Locate every Plasmodium ovale-infected red blood cell.
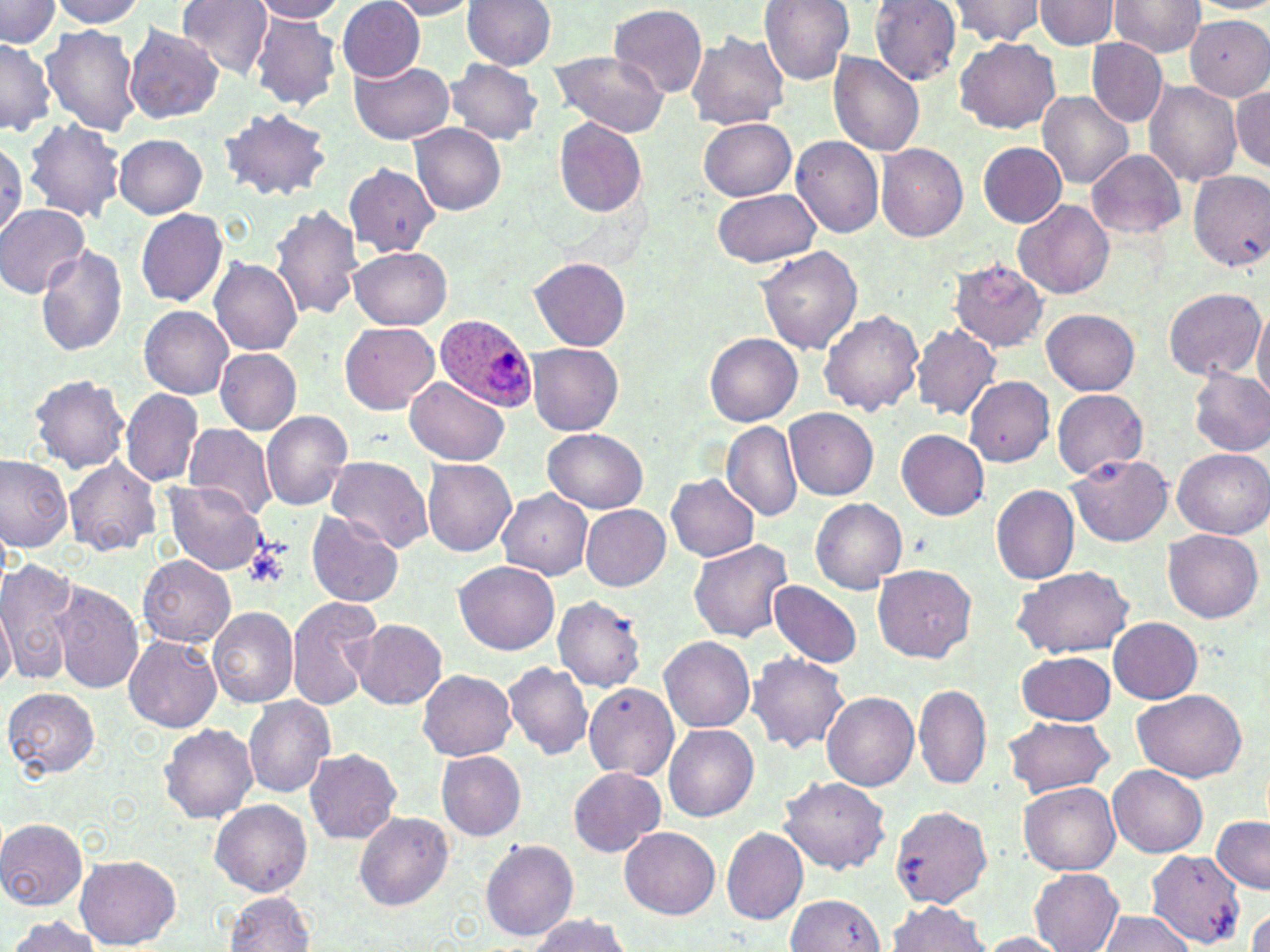

Approximate bounding boxes as named x1/y1/x2/y2 corners in pixels.
Plasmodium ovale-infected red blood cells: (x1=432, y1=313, x2=535, y2=414).

Uninfected red blood cell locations: (x1=176, y1=0, x2=274, y2=78), (x1=250, y1=0, x2=348, y2=23), (x1=383, y1=0, x2=482, y2=20), (x1=461, y1=0, x2=556, y2=70), (x1=759, y1=0, x2=855, y2=84), (x1=942, y1=0, x2=1049, y2=46), (x1=0, y1=1, x2=61, y2=49), (x1=49, y1=1, x2=148, y2=28), (x1=337, y1=1, x2=425, y2=81), (x1=870, y1=1, x2=962, y2=84), (x1=1035, y1=1, x2=1121, y2=49), (x1=1109, y1=1, x2=1205, y2=58), (x1=1187, y1=1, x2=1270, y2=14), (x1=609, y1=4, x2=708, y2=99), (x1=251, y1=6, x2=427, y2=99), (x1=249, y1=12, x2=341, y2=111), (x1=1185, y1=15, x2=1269, y2=99), (x1=41, y1=24, x2=142, y2=136), (x1=123, y1=24, x2=225, y2=124), (x1=686, y1=31, x2=789, y2=132), (x1=0, y1=37, x2=55, y2=136), (x1=954, y1=37, x2=1059, y2=133), (x1=1087, y1=39, x2=1167, y2=127), (x1=547, y1=48, x2=672, y2=137), (x1=828, y1=52, x2=926, y2=155), (x1=446, y1=59, x2=543, y2=145), (x1=352, y1=61, x2=454, y2=143), (x1=1143, y1=81, x2=1243, y2=186), (x1=1231, y1=86, x2=1270, y2=170), (x1=1039, y1=91, x2=1133, y2=190), (x1=217, y1=108, x2=333, y2=202), (x1=23, y1=117, x2=124, y2=220), (x1=699, y1=118, x2=797, y2=201), (x1=554, y1=119, x2=648, y2=216), (x1=410, y1=123, x2=506, y2=215), (x1=113, y1=134, x2=207, y2=218), (x1=789, y1=136, x2=884, y2=239), (x1=0, y1=138, x2=24, y2=236), (x1=978, y1=142, x2=1066, y2=226), (x1=876, y1=143, x2=968, y2=242), (x1=1087, y1=149, x2=1185, y2=240), (x1=343, y1=163, x2=440, y2=258), (x1=1188, y1=171, x2=1270, y2=272), (x1=710, y1=190, x2=821, y2=267), (x1=1013, y1=199, x2=1113, y2=300), (x1=0, y1=202, x2=91, y2=298), (x1=270, y1=204, x2=366, y2=321), (x1=135, y1=208, x2=227, y2=308), (x1=36, y1=245, x2=128, y2=356), (x1=756, y1=246, x2=862, y2=355), (x1=349, y1=247, x2=451, y2=329), (x1=209, y1=258, x2=302, y2=356), (x1=531, y1=258, x2=632, y2=350), (x1=949, y1=259, x2=1049, y2=353), (x1=1162, y1=287, x2=1267, y2=383), (x1=1252, y1=304, x2=1270, y2=407), (x1=139, y1=306, x2=232, y2=400), (x1=818, y1=309, x2=923, y2=415), (x1=1042, y1=309, x2=1139, y2=394), (x1=341, y1=322, x2=439, y2=415), (x1=911, y1=323, x2=1001, y2=421), (x1=704, y1=331, x2=802, y2=426), (x1=526, y1=344, x2=623, y2=436), (x1=215, y1=348, x2=302, y2=434), (x1=1189, y1=368, x2=1270, y2=456), (x1=26, y1=373, x2=131, y2=473), (x1=405, y1=376, x2=508, y2=465), (x1=963, y1=377, x2=1053, y2=466), (x1=121, y1=389, x2=205, y2=486), (x1=1052, y1=389, x2=1149, y2=479), (x1=785, y1=408, x2=878, y2=498), (x1=260, y1=411, x2=354, y2=511), (x1=723, y1=421, x2=800, y2=520), (x1=181, y1=422, x2=277, y2=521), (x1=543, y1=428, x2=648, y2=513), (x1=897, y1=430, x2=989, y2=520), (x1=1173, y1=449, x2=1269, y2=538), (x1=0, y1=453, x2=72, y2=552), (x1=324, y1=455, x2=433, y2=554), (x1=1068, y1=455, x2=1172, y2=545), (x1=64, y1=458, x2=162, y2=556), (x1=423, y1=458, x2=516, y2=557), (x1=666, y1=473, x2=759, y2=562), (x1=166, y1=482, x2=265, y2=574), (x1=992, y1=485, x2=1081, y2=582), (x1=497, y1=489, x2=593, y2=580), (x1=810, y1=498, x2=907, y2=594), (x1=581, y1=505, x2=671, y2=591), (x1=307, y1=512, x2=405, y2=608), (x1=1163, y1=529, x2=1263, y2=623), (x1=689, y1=539, x2=795, y2=642), (x1=137, y1=555, x2=234, y2=647), (x1=0, y1=559, x2=82, y2=683), (x1=454, y1=560, x2=558, y2=654), (x1=872, y1=564, x2=976, y2=662), (x1=1012, y1=565, x2=1133, y2=657), (x1=53, y1=582, x2=144, y2=693), (x1=768, y1=582, x2=862, y2=668), (x1=0, y1=593, x2=15, y2=693), (x1=286, y1=596, x2=382, y2=710), (x1=554, y1=596, x2=650, y2=691), (x1=206, y1=606, x2=298, y2=707), (x1=1109, y1=616, x2=1203, y2=703), (x1=352, y1=619, x2=447, y2=710), (x1=124, y1=636, x2=221, y2=732), (x1=659, y1=636, x2=755, y2=734), (x1=1015, y1=651, x2=1117, y2=725), (x1=746, y1=652, x2=851, y2=753), (x1=504, y1=661, x2=594, y2=759), (x1=419, y1=668, x2=517, y2=761), (x1=912, y1=683, x2=991, y2=790), (x1=583, y1=684, x2=680, y2=780), (x1=4, y1=687, x2=100, y2=778), (x1=1130, y1=687, x2=1246, y2=782), (x1=821, y1=691, x2=918, y2=791), (x1=243, y1=695, x2=336, y2=800), (x1=1004, y1=716, x2=1113, y2=797), (x1=161, y1=723, x2=258, y2=823), (x1=663, y1=724, x2=759, y2=821), (x1=303, y1=748, x2=402, y2=845), (x1=436, y1=750, x2=526, y2=840), (x1=1109, y1=765, x2=1208, y2=858), (x1=568, y1=766, x2=665, y2=857), (x1=778, y1=777, x2=891, y2=875), (x1=1020, y1=782, x2=1120, y2=876), (x1=211, y1=799, x2=313, y2=896), (x1=891, y1=805, x2=991, y2=908), (x1=353, y1=810, x2=455, y2=912), (x1=1211, y1=817, x2=1269, y2=893), (x1=0, y1=818, x2=89, y2=911), (x1=620, y1=827, x2=720, y2=919), (x1=721, y1=827, x2=808, y2=925), (x1=481, y1=839, x2=580, y2=940), (x1=1147, y1=849, x2=1245, y2=947), (x1=74, y1=854, x2=181, y2=948), (x1=1029, y1=869, x2=1124, y2=952), (x1=224, y1=891, x2=316, y2=951), (x1=787, y1=894, x2=885, y2=950), (x1=886, y1=900, x2=990, y2=951), (x1=1246, y1=905, x2=1270, y2=952), (x1=1097, y1=909, x2=1198, y2=952), (x1=528, y1=913, x2=631, y2=951), (x1=5, y1=916, x2=102, y2=952), (x1=977, y1=932, x2=1073, y2=951). Platelet locations: (x1=243, y1=541, x2=291, y2=590). Slide-level diagnosis: Plasmodium ovale. Thin blood film. 1000x magnification. Image is 1270×952 pixels. May-Grünwald-Giemsa-stained preparation. Optical microscopy. Single field of view.